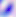 Photomicrograph. Toxoplasma gondii is shown. 400x magnification.